Point out each Plasmodium parasite.
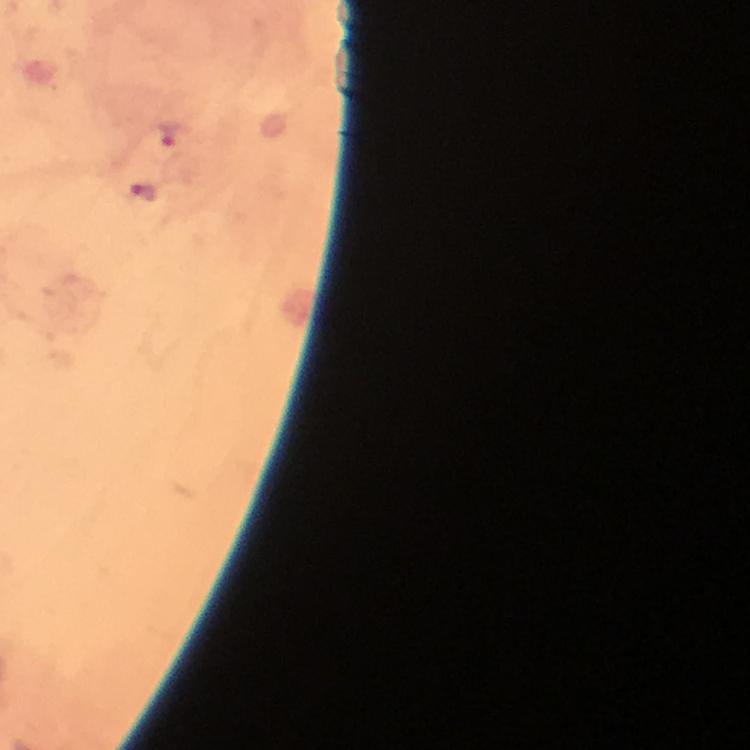

Approximate centers as (x, y) in pixels.
Plasmodium parasites: (167, 136), (144, 192).

stain: Giemsa
capture: smartphone mounted on the microscope
context: from a malaria diagnostic workup
magnification: 100x
preparation: thick blood film
image_size: 750×750 pixels
cropped_from: one field of view
immersion_oil: used